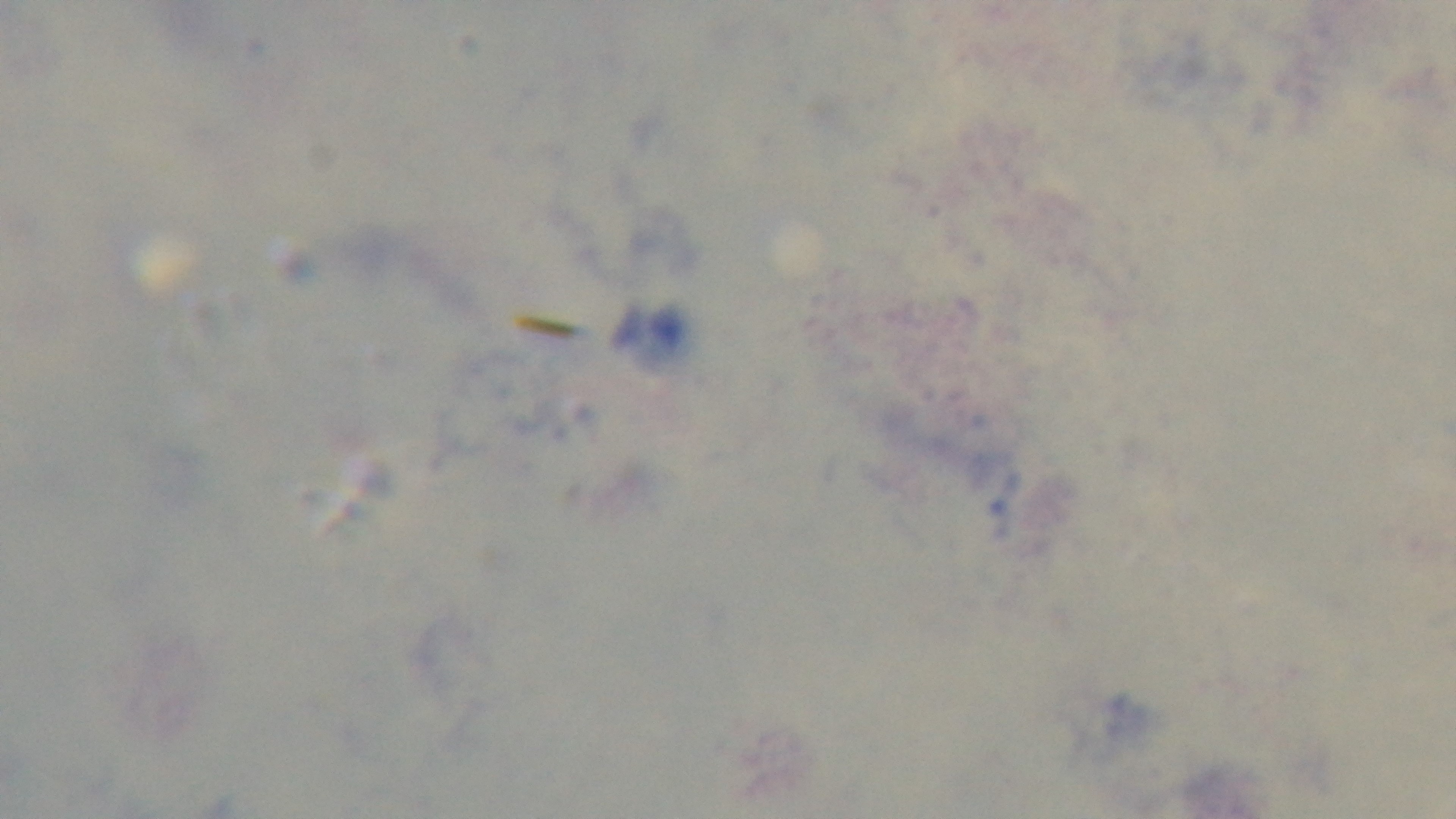
Summary:
  - Modality: light microscopy
  - Field of view: one from the slide
  - Objective: 100x oil immersion
  - Preparation: thick
  - Stain: Giemsa
  - Capture: mounted 4K digital camera
  - Malaria status: negative